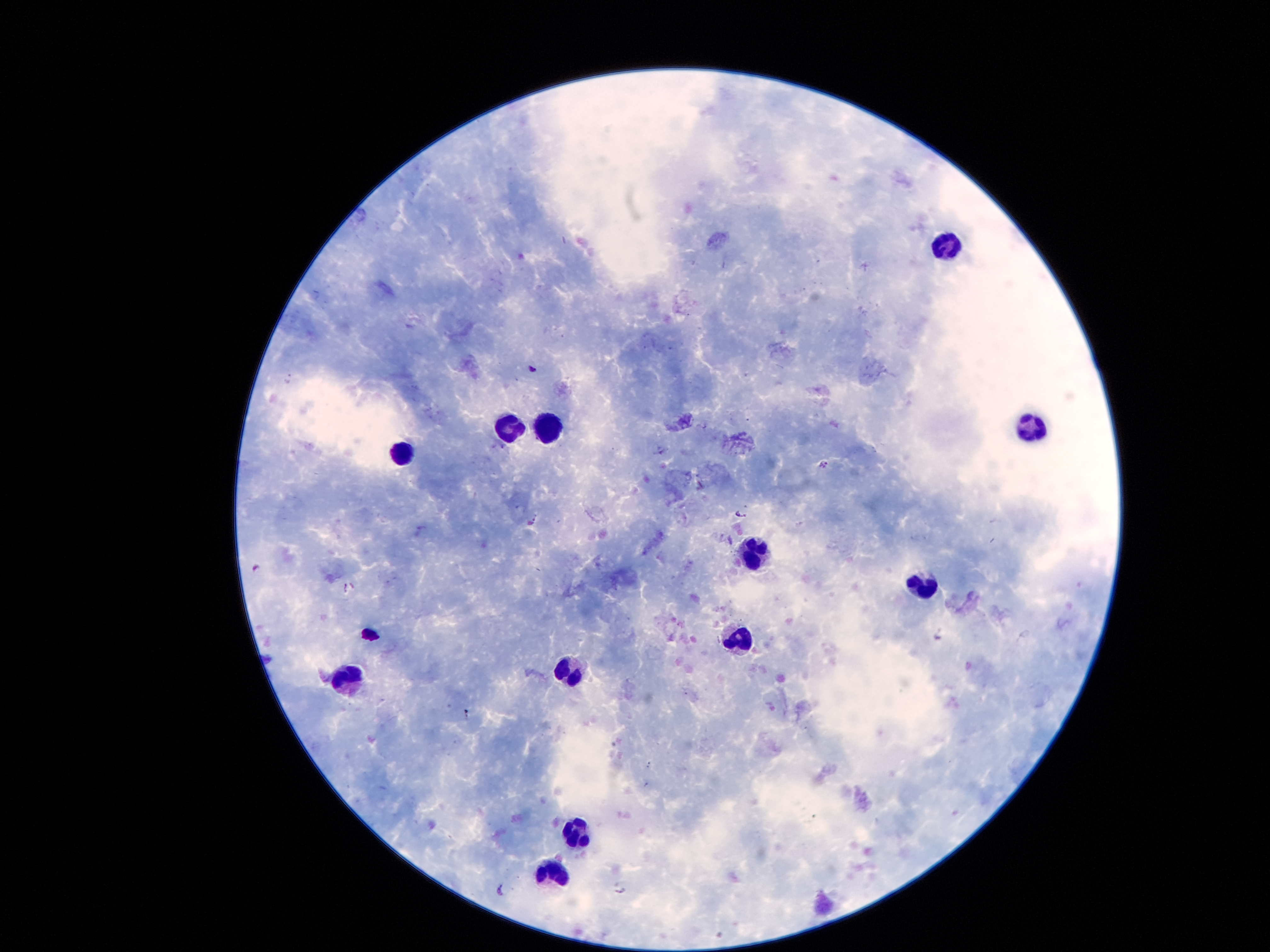 Approximate object centers, in pixels from the top-left corner. Leukocyte locations: (x=948, y=252), (x=505, y=426), (x=1029, y=426), (x=550, y=431), (x=399, y=455), (x=754, y=554), (x=920, y=588), (x=740, y=635), (x=569, y=671), (x=345, y=680), (x=575, y=831), (x=553, y=873). Malaria parasite locations: (x=531, y=368), (x=660, y=452), (x=825, y=465), (x=740, y=514), (x=533, y=520), (x=346, y=587), (x=649, y=765), (x=500, y=889), (x=618, y=889). Single field of view. Photographed through the microscope eyepiece with a smartphone camera. Patient malaria status: infected with Plasmodium falciparum. Image is 1270×952 pixels. Thick peripheral-blood smear. Giemsa stain. 100x magnification.